Comment on the morphology of the erythrocytes.
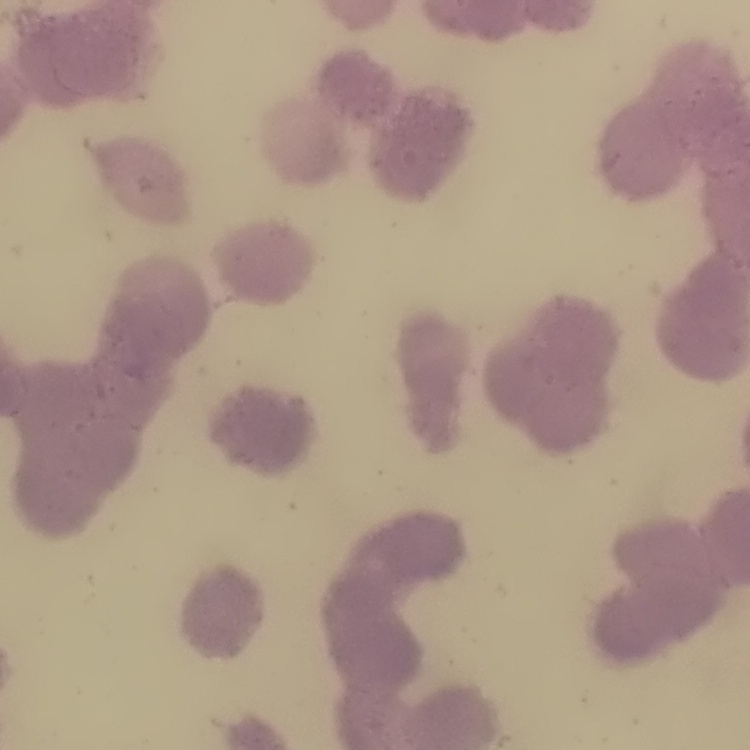
Rouleaux formation.

stain: Field's or Giemsa
image_type: one tile cut from a larger photomicrograph
preparation: thin blood film